Look for Plasmodium parasites.
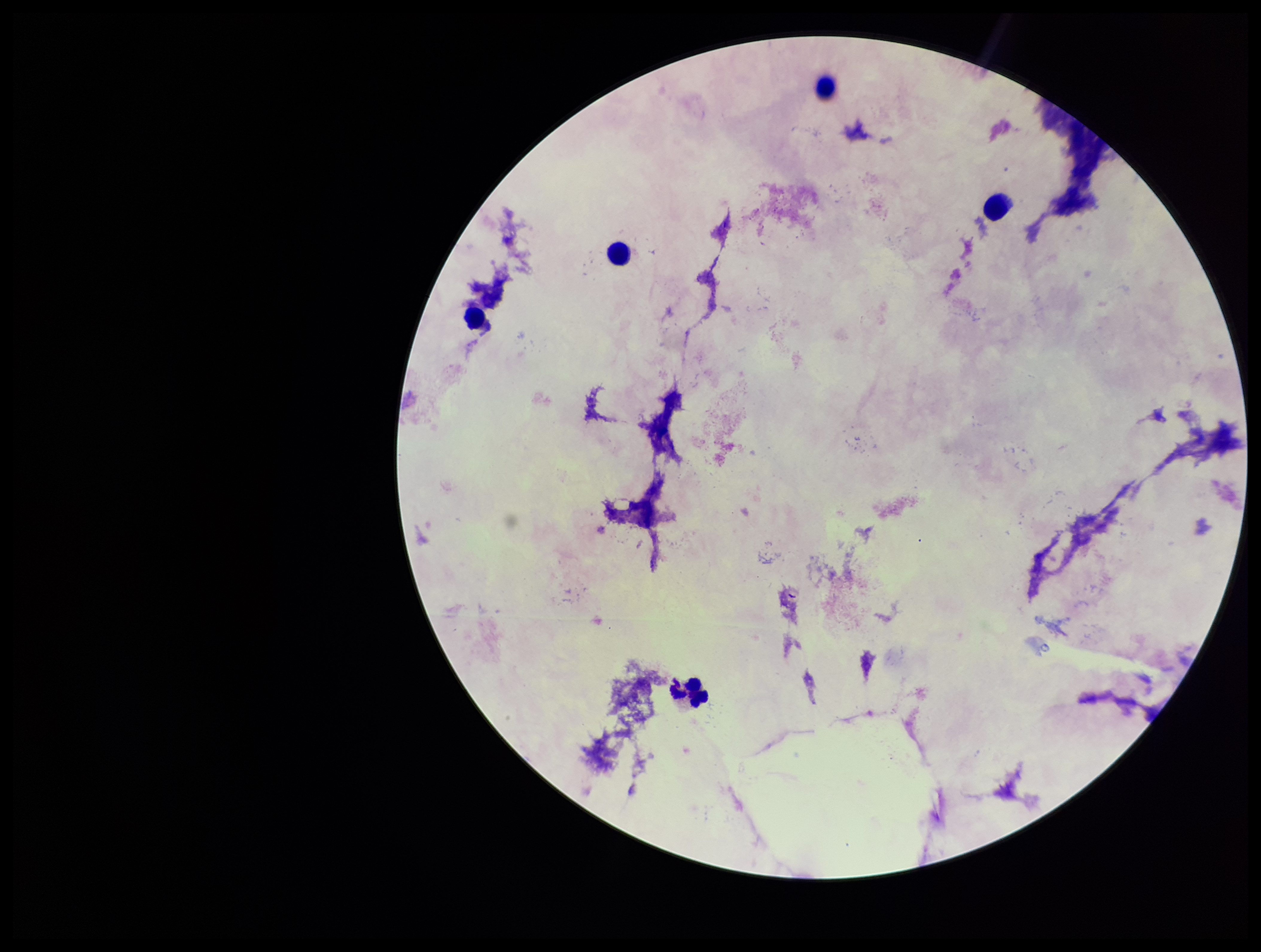
None seen.

{
  "capture": "smartphone photograph through the microscope eyepiece",
  "stain": "Giemsa",
  "preparation": "thick smear",
  "image_size": "1261×952 pixels",
  "patient_malaria_status": "negative",
  "leukocyte_count": 5,
  "field_of_view": "single",
  "parasite_count": 0
}